Locate every malaria parasite.
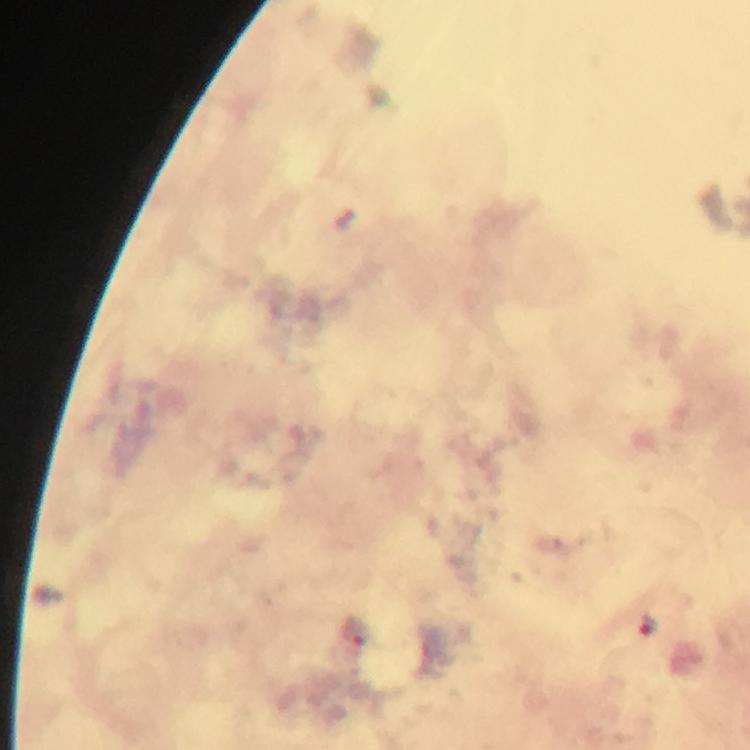

Approximate centers as {x, y} in pixels.
Malaria parasites: {648, 622}, {356, 632}.

Image is 750×750 pixels. A crop from one field of view. Immersion oil was used. At 100x magnification. Photographed through the microscope with a smartphone camera. Giemsa-stained preparation. Thick smear. From a malaria diagnostic workup.